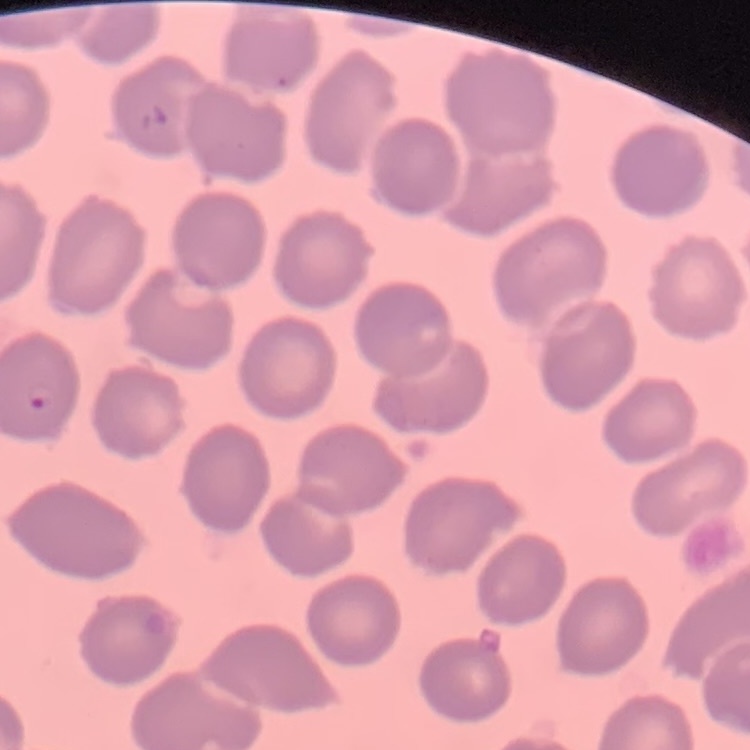
erythrocyte morphology = no rouleaux formation
preparation = thin peripheral smear
image type = one tile cut from a larger photomicrograph
stain = Field's or Giemsa